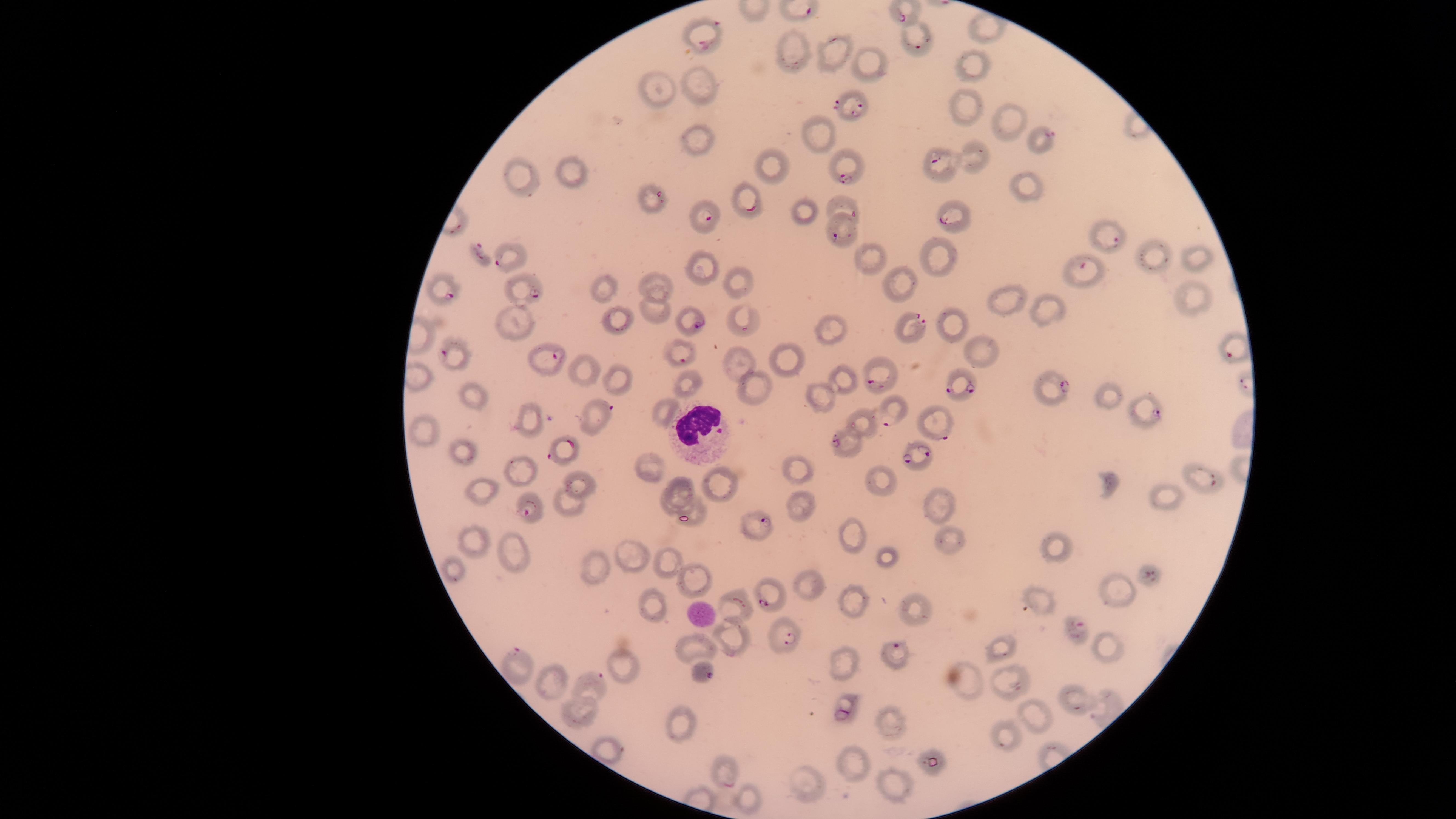
Approximate marker points, in pixels from the top-left corner.
Summary:
  - White blood cells: (x=703, y=430)
  - Uninfected red blood cells: (x=789, y=50), (x=832, y=59), (x=974, y=63), (x=871, y=65), (x=704, y=87), (x=660, y=90), (x=966, y=110), (x=1010, y=120), (x=820, y=135), (x=698, y=144), (x=974, y=160), (x=770, y=171), (x=568, y=175), (x=515, y=186), (x=1024, y=188), (x=807, y=216), (x=939, y=253), (x=1155, y=254), (x=866, y=258), (x=1195, y=259), (x=698, y=269), (x=898, y=282), (x=657, y=283), (x=742, y=284), (x=604, y=288), (x=1191, y=295), (x=1005, y=301), (x=651, y=309), (x=1048, y=309), (x=512, y=318), (x=747, y=318), (x=614, y=320), (x=952, y=325), (x=831, y=331), (x=981, y=347), (x=738, y=359), (x=787, y=361), (x=583, y=370), (x=843, y=380), (x=622, y=381), (x=690, y=384), (x=749, y=387), (x=474, y=395), (x=1108, y=398), (x=820, y=400), (x=661, y=411), (x=524, y=418), (x=862, y=423), (x=425, y=429), (x=845, y=449), (x=463, y=453), (x=646, y=466), (x=798, y=469), (x=515, y=474), (x=882, y=480), (x=1108, y=483), (x=574, y=485), (x=721, y=485), (x=479, y=489), (x=679, y=490), (x=940, y=502), (x=1166, y=504), (x=567, y=506), (x=798, y=506), (x=667, y=508), (x=694, y=508), (x=850, y=536), (x=950, y=541), (x=476, y=546), (x=515, y=546), (x=1060, y=549), (x=629, y=555), (x=888, y=558), (x=670, y=563), (x=450, y=569), (x=595, y=573), (x=697, y=579), (x=808, y=581), (x=1110, y=586), (x=1041, y=598), (x=853, y=602), (x=736, y=606), (x=912, y=606), (x=656, y=607), (x=731, y=636), (x=698, y=647), (x=1003, y=649), (x=1108, y=650), (x=847, y=656), (x=627, y=661), (x=554, y=678), (x=1010, y=681), (x=962, y=682), (x=1078, y=702), (x=1040, y=713), (x=586, y=717), (x=893, y=725), (x=686, y=727), (x=1010, y=733), (x=609, y=749), (x=853, y=762), (x=811, y=784), (x=894, y=787), (x=745, y=795)
  - Parasitized red blood cells: (x=712, y=27), (x=915, y=45), (x=859, y=107), (x=1043, y=137), (x=934, y=160), (x=847, y=175), (x=753, y=210), (x=855, y=213), (x=706, y=218), (x=945, y=220), (x=833, y=237), (x=1114, y=239), (x=508, y=251), (x=481, y=253), (x=1086, y=265), (x=531, y=294), (x=454, y=298), (x=695, y=322), (x=916, y=323), (x=1230, y=348), (x=457, y=352), (x=553, y=357), (x=685, y=359), (x=881, y=379), (x=964, y=385), (x=1059, y=390), (x=603, y=408), (x=1149, y=415), (x=885, y=420), (x=941, y=426), (x=917, y=452), (x=552, y=457), (x=1210, y=482), (x=529, y=512), (x=762, y=522), (x=1151, y=576), (x=771, y=602), (x=1080, y=624), (x=785, y=639), (x=896, y=648), (x=518, y=656), (x=704, y=672), (x=597, y=678), (x=844, y=711), (x=728, y=784)
  - Species: Plasmodium falciparum
  - Visible region: circular
  - Field of view: single
  - Presence: malaria parasites detected
  - Stain: Giemsa
  - Preparation: thin blood smear
  - Image size: 1456×819 pixels
  - Capture: smartphone photograph through the microscope eyepiece